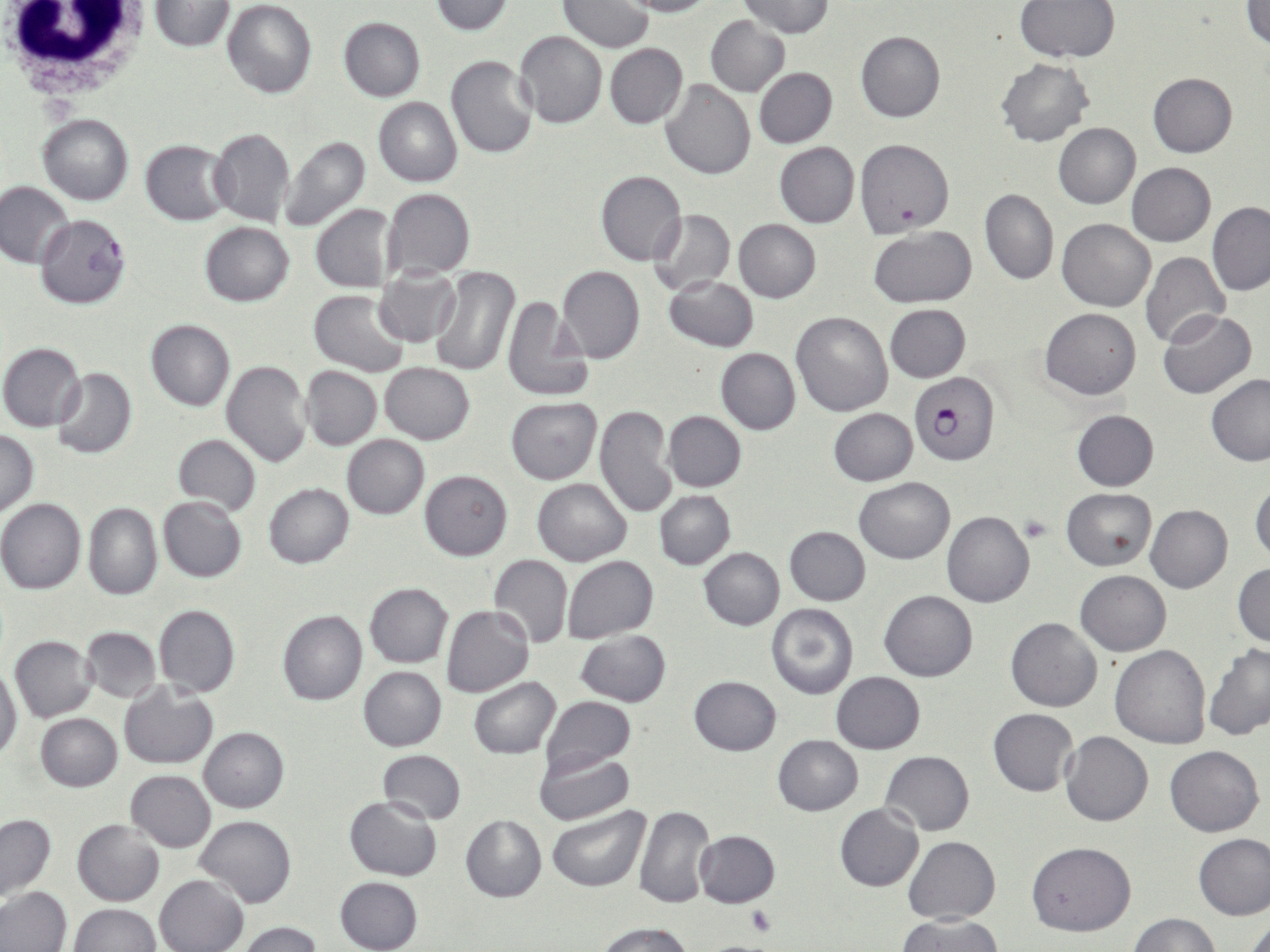
Approximate bounding boxes as named x1/y1/x2/y2 corners in pixels. Plasmodium falciparum-infected red blood cell locations: (x1=36, y1=214, x2=131, y2=309), (x1=910, y1=371, x2=1001, y2=467). White blood cell locations: (x1=0, y1=1, x2=152, y2=104). Platelet locations: (x1=1023, y1=516, x2=1051, y2=541), (x1=744, y1=903, x2=776, y2=938), (x1=702, y1=941, x2=769, y2=951). Uninfected red blood cell locations: (x1=149, y1=0, x2=234, y2=51), (x1=222, y1=0, x2=317, y2=99), (x1=429, y1=0, x2=515, y2=35), (x1=622, y1=0, x2=715, y2=17), (x1=739, y1=0, x2=836, y2=38), (x1=558, y1=1, x2=654, y2=52), (x1=1016, y1=1, x2=1119, y2=62), (x1=1244, y1=1, x2=1270, y2=48), (x1=706, y1=14, x2=790, y2=96), (x1=339, y1=17, x2=426, y2=101), (x1=514, y1=30, x2=607, y2=128), (x1=856, y1=31, x2=946, y2=122), (x1=605, y1=43, x2=687, y2=128), (x1=445, y1=54, x2=538, y2=160), (x1=996, y1=57, x2=1094, y2=147), (x1=754, y1=68, x2=837, y2=147), (x1=1148, y1=73, x2=1237, y2=157), (x1=659, y1=81, x2=756, y2=181), (x1=373, y1=96, x2=462, y2=187), (x1=38, y1=113, x2=134, y2=205), (x1=1053, y1=122, x2=1141, y2=208), (x1=207, y1=127, x2=295, y2=227), (x1=278, y1=135, x2=371, y2=234), (x1=856, y1=138, x2=955, y2=237), (x1=139, y1=140, x2=235, y2=225), (x1=774, y1=142, x2=860, y2=228), (x1=1127, y1=162, x2=1216, y2=246), (x1=595, y1=171, x2=687, y2=265), (x1=0, y1=182, x2=74, y2=269), (x1=382, y1=189, x2=475, y2=279), (x1=980, y1=189, x2=1058, y2=286), (x1=1207, y1=202, x2=1270, y2=295), (x1=310, y1=203, x2=400, y2=293), (x1=648, y1=209, x2=735, y2=297), (x1=1057, y1=217, x2=1154, y2=311), (x1=733, y1=218, x2=822, y2=302), (x1=200, y1=222, x2=293, y2=307), (x1=869, y1=226, x2=976, y2=308), (x1=1140, y1=250, x2=1230, y2=348), (x1=428, y1=265, x2=518, y2=377), (x1=556, y1=266, x2=645, y2=364), (x1=374, y1=267, x2=460, y2=346), (x1=663, y1=275, x2=759, y2=351), (x1=309, y1=290, x2=411, y2=377), (x1=500, y1=296, x2=593, y2=401), (x1=884, y1=305, x2=969, y2=382), (x1=1040, y1=307, x2=1140, y2=399), (x1=1158, y1=308, x2=1258, y2=399), (x1=791, y1=310, x2=893, y2=417), (x1=145, y1=319, x2=235, y2=411), (x1=1, y1=342, x2=86, y2=431), (x1=715, y1=348, x2=800, y2=435), (x1=220, y1=359, x2=312, y2=467), (x1=379, y1=362, x2=474, y2=444), (x1=300, y1=366, x2=382, y2=451), (x1=51, y1=369, x2=137, y2=459), (x1=1205, y1=374, x2=1270, y2=466), (x1=506, y1=398, x2=602, y2=484), (x1=595, y1=404, x2=677, y2=519), (x1=829, y1=407, x2=918, y2=485), (x1=663, y1=410, x2=746, y2=492), (x1=1071, y1=410, x2=1158, y2=491), (x1=0, y1=429, x2=39, y2=516), (x1=172, y1=435, x2=262, y2=516), (x1=341, y1=435, x2=428, y2=519), (x1=420, y1=470, x2=513, y2=560), (x1=853, y1=477, x2=955, y2=564), (x1=532, y1=478, x2=632, y2=565), (x1=1249, y1=478, x2=1270, y2=564), (x1=264, y1=483, x2=353, y2=568), (x1=1061, y1=488, x2=1155, y2=570), (x1=654, y1=491, x2=736, y2=569), (x1=157, y1=496, x2=247, y2=582), (x1=0, y1=498, x2=86, y2=593), (x1=82, y1=501, x2=163, y2=601), (x1=1145, y1=504, x2=1233, y2=593), (x1=942, y1=511, x2=1034, y2=607), (x1=785, y1=526, x2=871, y2=605), (x1=699, y1=548, x2=785, y2=630), (x1=488, y1=555, x2=573, y2=648), (x1=562, y1=556, x2=659, y2=642), (x1=1232, y1=563, x2=1270, y2=647), (x1=1076, y1=571, x2=1170, y2=656), (x1=364, y1=583, x2=452, y2=668), (x1=880, y1=589, x2=978, y2=681), (x1=766, y1=603, x2=858, y2=699), (x1=153, y1=604, x2=239, y2=696), (x1=441, y1=605, x2=534, y2=696), (x1=277, y1=610, x2=367, y2=705), (x1=1005, y1=617, x2=1101, y2=711), (x1=80, y1=626, x2=161, y2=701), (x1=575, y1=630, x2=672, y2=706), (x1=9, y1=636, x2=97, y2=722), (x1=1203, y1=643, x2=1270, y2=741), (x1=1109, y1=645, x2=1211, y2=749), (x1=0, y1=662, x2=22, y2=763), (x1=357, y1=666, x2=446, y2=752), (x1=831, y1=671, x2=924, y2=754), (x1=468, y1=677, x2=561, y2=758), (x1=688, y1=677, x2=780, y2=756), (x1=119, y1=681, x2=219, y2=770), (x1=540, y1=695, x2=636, y2=773), (x1=988, y1=707, x2=1078, y2=796), (x1=35, y1=713, x2=123, y2=792), (x1=198, y1=726, x2=288, y2=813), (x1=1061, y1=731, x2=1153, y2=826), (x1=773, y1=734, x2=863, y2=815), (x1=1165, y1=745, x2=1264, y2=836), (x1=533, y1=748, x2=633, y2=825), (x1=377, y1=750, x2=466, y2=824), (x1=880, y1=750, x2=974, y2=835), (x1=126, y1=770, x2=216, y2=852), (x1=344, y1=797, x2=442, y2=880), (x1=834, y1=803, x2=924, y2=892), (x1=634, y1=805, x2=714, y2=910), (x1=547, y1=806, x2=648, y2=892), (x1=0, y1=813, x2=56, y2=904), (x1=461, y1=815, x2=547, y2=901), (x1=195, y1=816, x2=297, y2=908), (x1=72, y1=820, x2=164, y2=906), (x1=693, y1=830, x2=780, y2=907), (x1=1194, y1=834, x2=1270, y2=920), (x1=903, y1=835, x2=999, y2=925), (x1=1027, y1=840, x2=1136, y2=937), (x1=155, y1=874, x2=247, y2=952), (x1=334, y1=877, x2=423, y2=952), (x1=0, y1=886, x2=70, y2=952), (x1=67, y1=903, x2=160, y2=952), (x1=1130, y1=914, x2=1218, y2=952), (x1=898, y1=915, x2=1001, y2=952), (x1=1243, y1=917, x2=1270, y2=952), (x1=238, y1=921, x2=323, y2=952), (x1=597, y1=921, x2=692, y2=952). Slide-level diagnosis: Plasmodium falciparum. Image is 1270×952 pixels. May-Grünwald-Giemsa-stained preparation. Captured at 1000x magnification. Single field of view. Light microscopy. Thin blood smear.